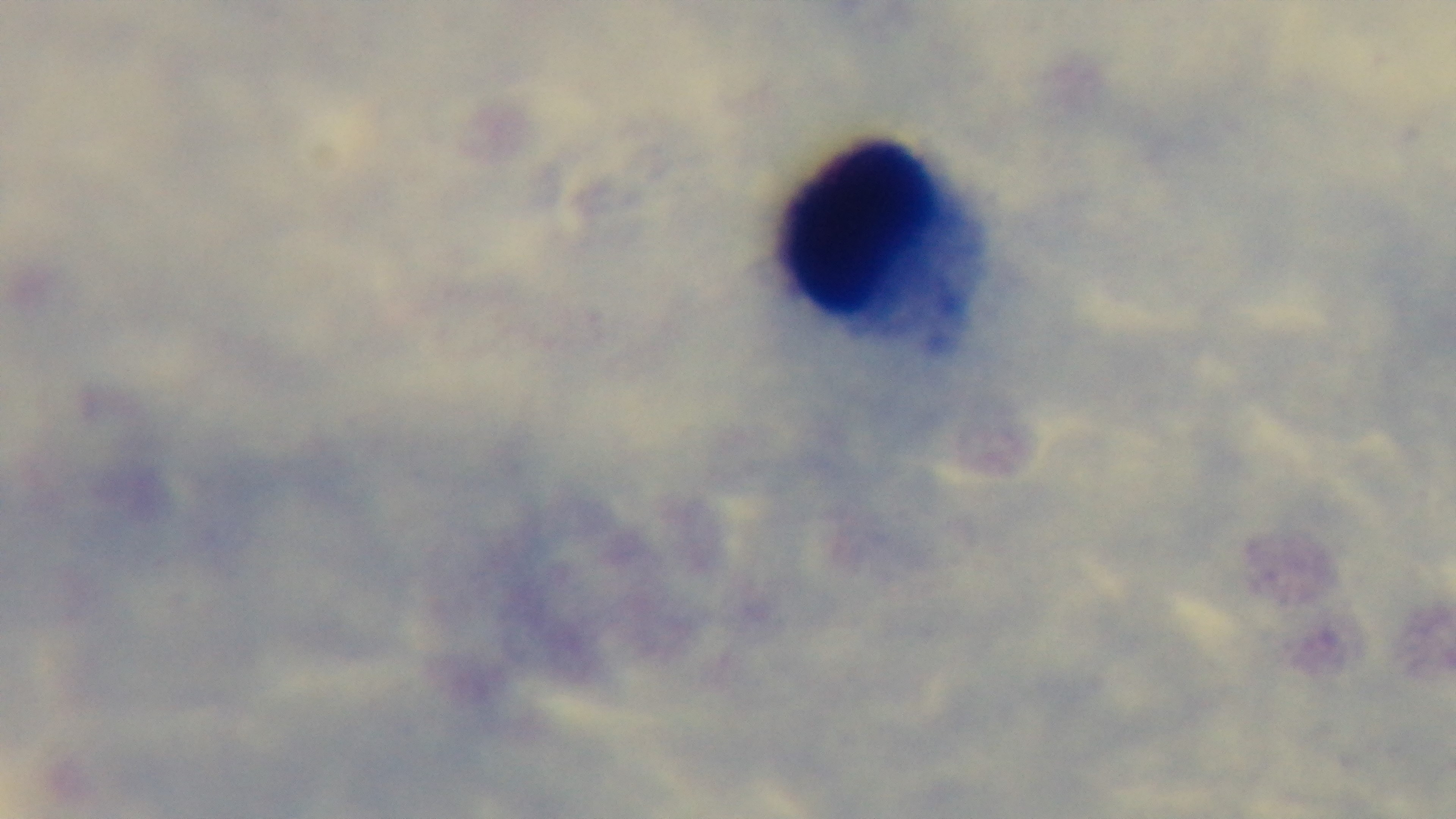
modality = light microscopy
stain = Giemsa
field of view = one from the slide
objective = 100x oil immersion
malaria status = negative
capture = mounted 4K digital camera
preparation = thick blood film